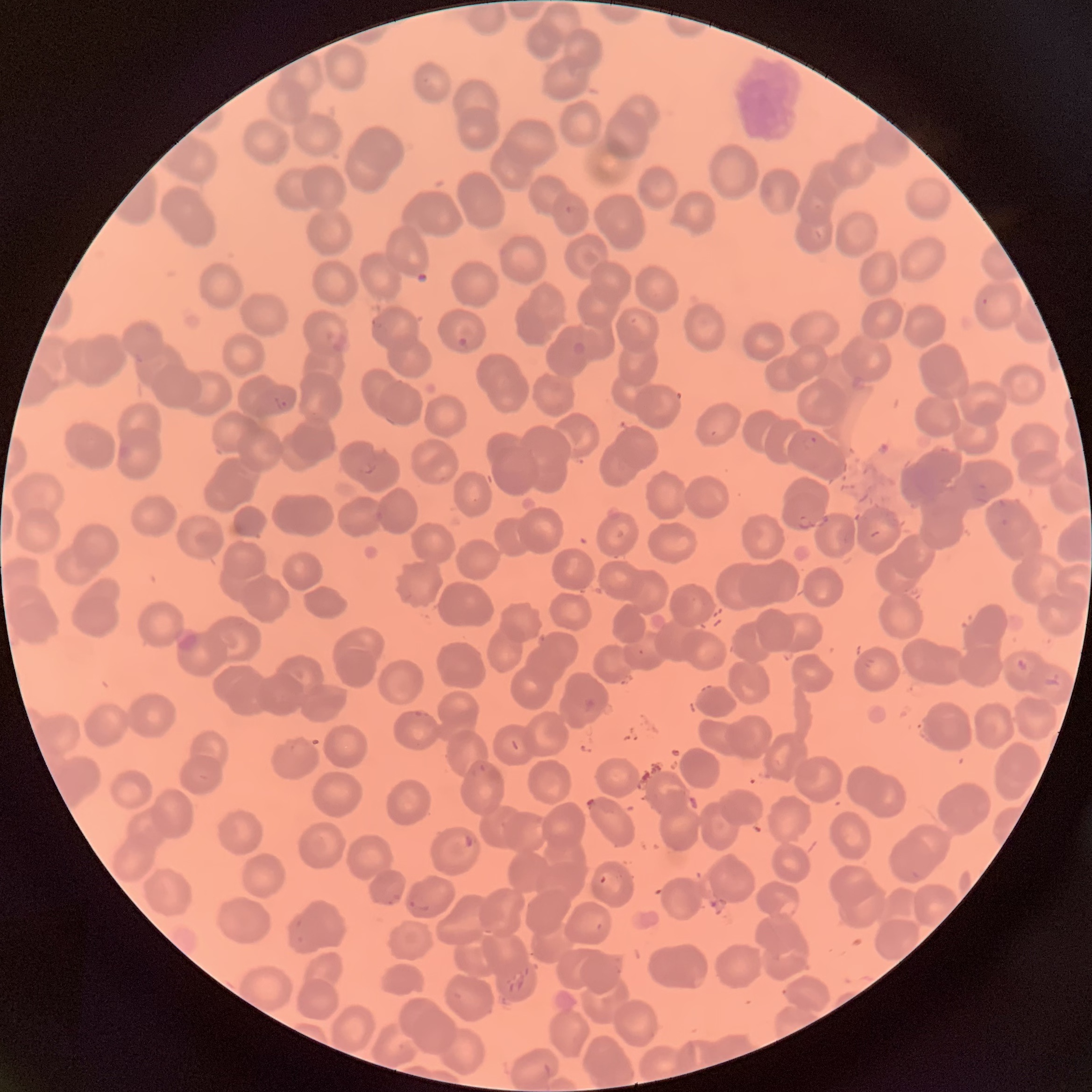
Approximate bounding boxes as [x1, y1, x2, y2] in pixels. Plasmodium parasite locations: [457, 336, 468, 348], [272, 396, 290, 411], [802, 435, 818, 450]. Image is 1092×1092 pixels. Light microscopy. The red blood cells show rouleaux formation. Thin blood smear.